Report the malaria status.
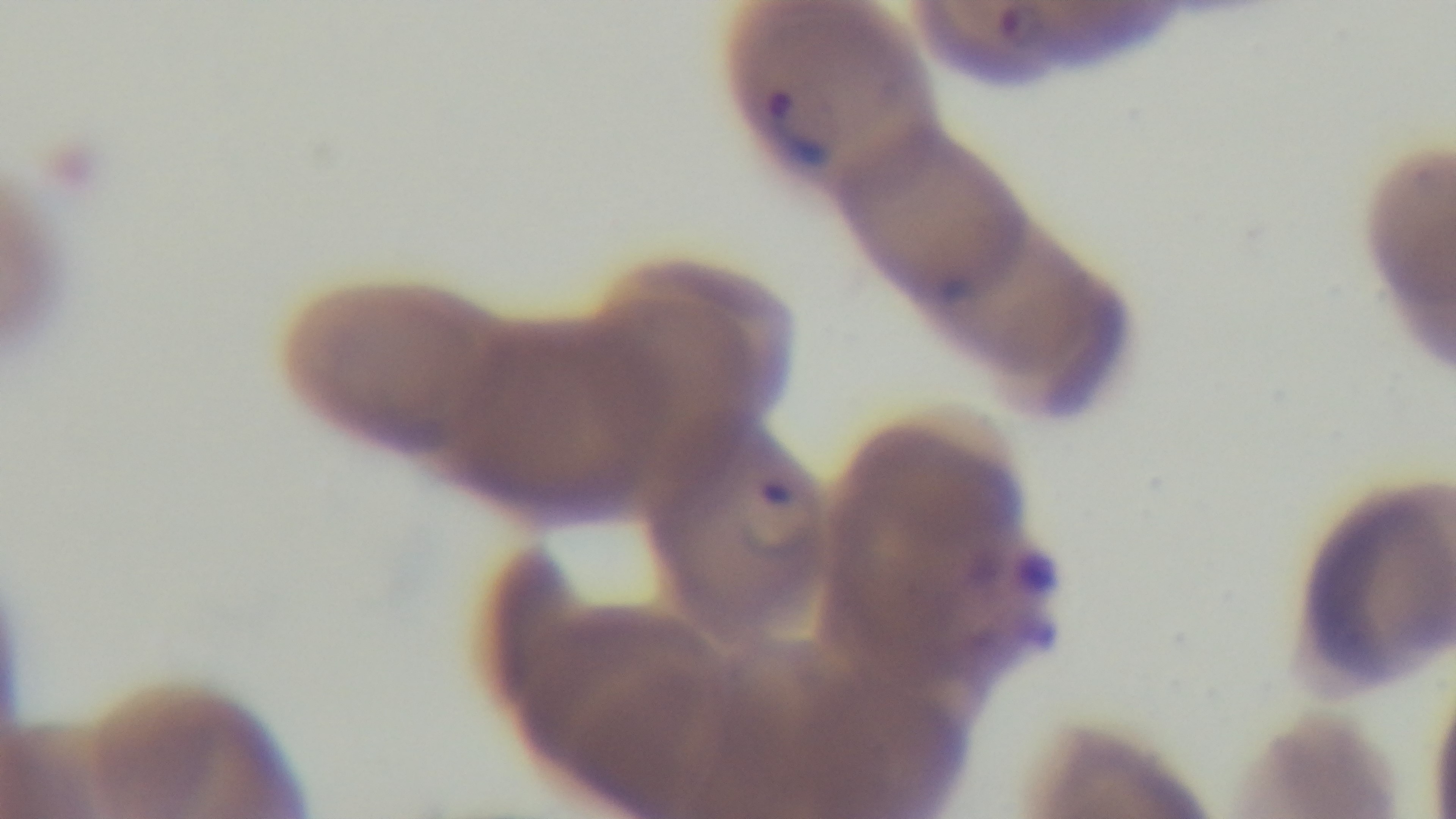
Infected.

Summary:
  - Capture: mounted 4K digital camera
  - Objective: 100x oil immersion
  - Preparation: thin blood film
  - Field of view: one from the slide
  - Stain: Giemsa
  - Modality: light microscopy